State which parasite is depicted.
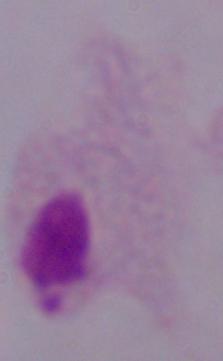

A trichomonad.

Summary:
  - Magnification: 1000x
  - Modality: photomicrograph